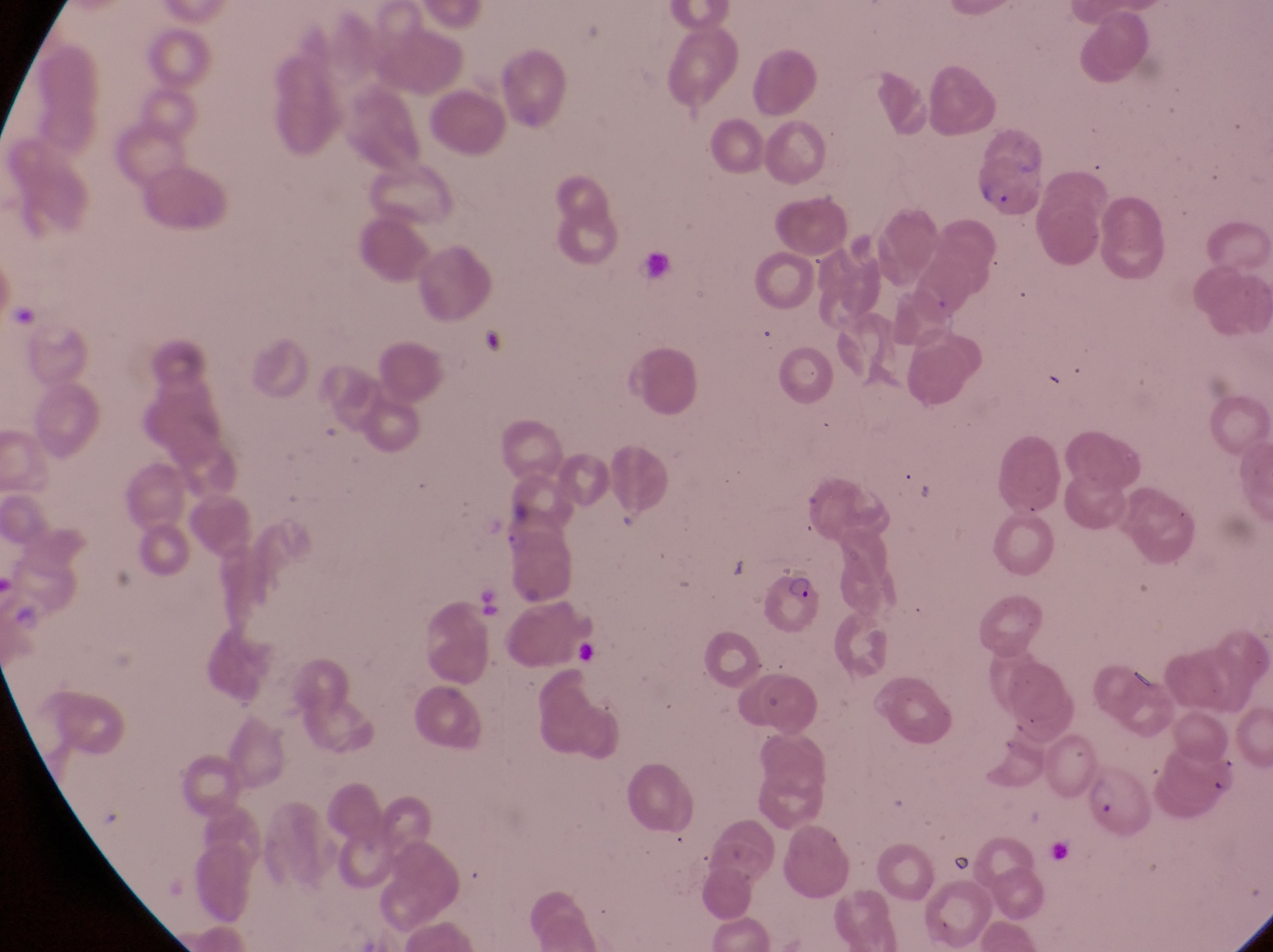 Approximate bounding boxes as (left, top, right, bottom) in pixels. Parasitised red blood cell locations: (976, 157, 1039, 219), (771, 569, 828, 643), (1086, 766, 1151, 848). Single field of view. Collected in Uganda. Thin blood smear. Captured by a smartphone held over the eyepiece of an Olympus CX-23 microscope. At a magnification of 1000x. Image is 1273×952 pixels.